Describe the morphology of the erythrocytes.
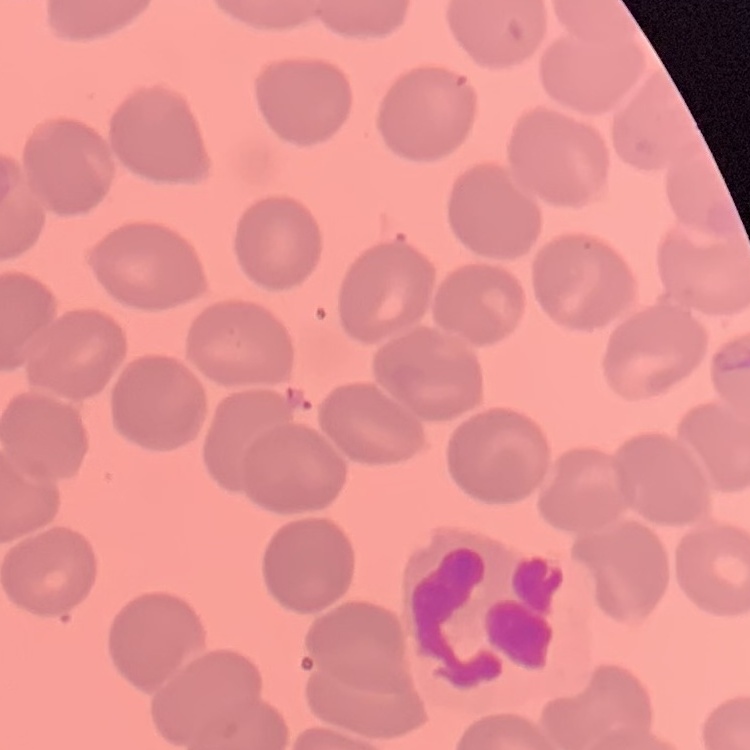

They show no rouleaux formation.

Thin blood film. Field's or Giemsa stain. Square crop of a larger photomicrograph.